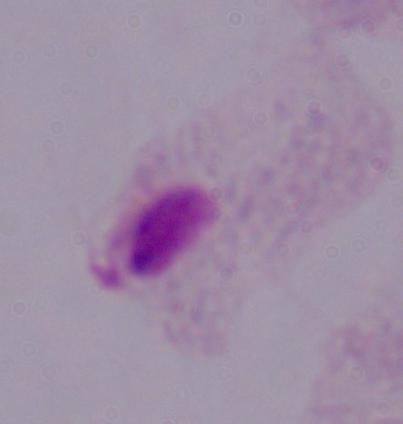

magnification = 1000x
modality = photomicrograph
identification = trichomonad